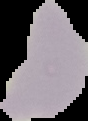

Summary:
  - Image type: cell region segmented out of the field of view; surrounding area masked to black
  - Preparation: thin blood smear
  - Image size: 88×121 pixels
  - Result: negative for malaria parasites